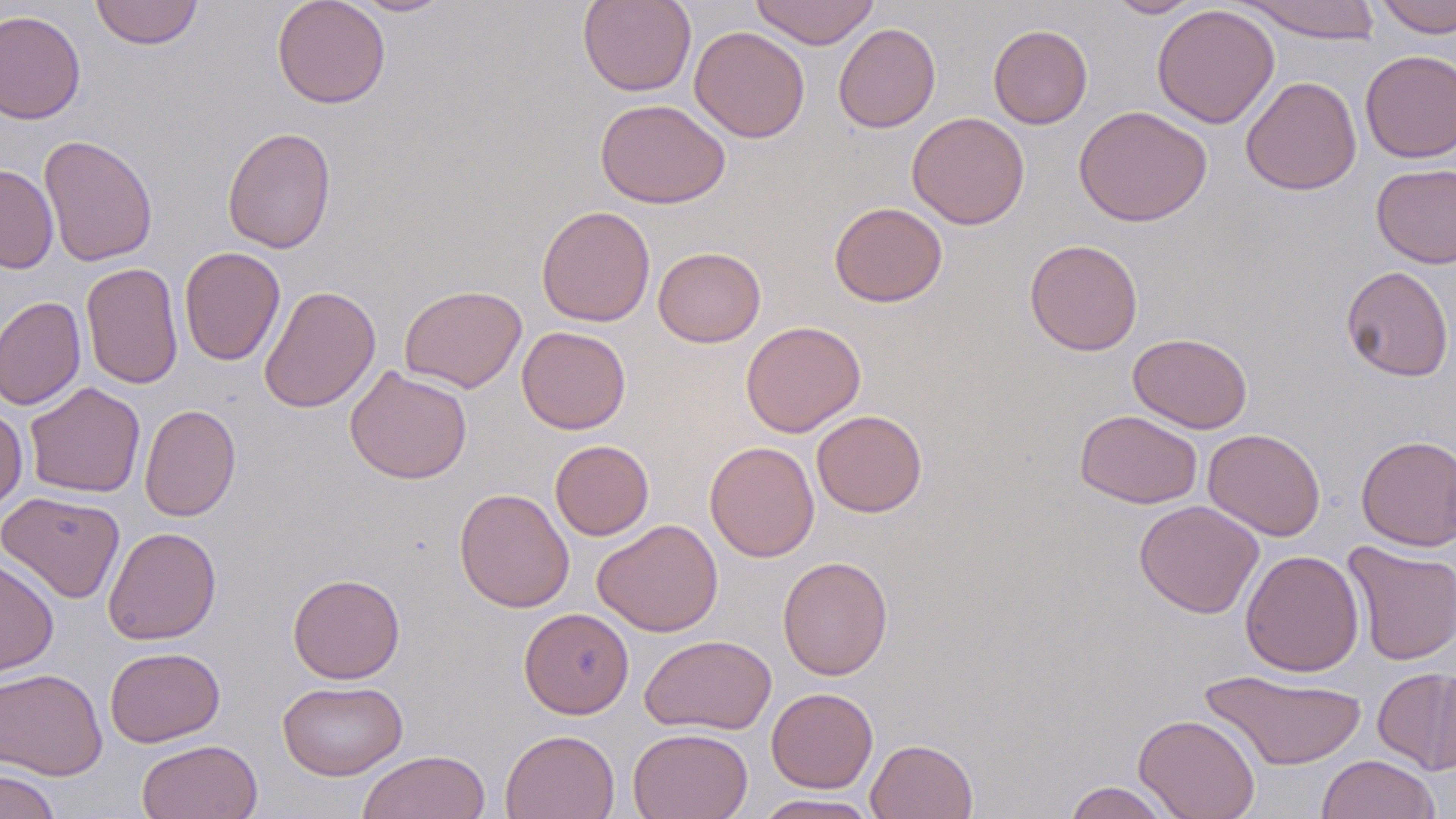
Summary:
  - Coordinate format: approximate bounding boxes as (x1,y1)-(x2,y2) corner pairs in pixels
  - Uninfected red blood cell locations: (89,0)-(204,49), (272,0)-(391,109), (348,0)-(456,16), (577,0)-(696,97), (750,0)-(880,49), (1106,0)-(1205,18), (1373,0)-(1456,37), (1235,1)-(1383,44), (1151,4)-(1280,129), (0,9)-(85,125), (833,23)-(941,133), (988,24)-(1092,129), (689,25)-(810,143), (1360,49)-(1456,163), (1240,75)-(1362,196), (595,98)-(731,208), (1073,105)-(1212,227), (906,112)-(1029,229), (222,126)-(337,254), (39,134)-(158,267), (1371,163)-(1456,269), (0,164)-(58,273), (829,201)-(947,307), (535,205)-(655,327), (1025,239)-(1143,356), (179,246)-(284,367), (653,246)-(766,348), (81,262)-(183,390), (1340,265)-(1454,382), (259,285)-(381,413), (399,285)-(527,393), (0,296)-(85,410), (740,320)-(866,438), (517,326)-(631,435), (1128,332)-(1253,433), (345,364)-(472,484), (24,381)-(145,498), (139,404)-(241,522), (0,406)-(28,511), (1075,409)-(1203,509), (811,410)-(927,517), (1203,428)-(1326,540), (1356,434)-(1456,551), (550,440)-(654,540), (704,441)-(820,562), (454,487)-(575,613), (0,491)-(126,603), (1134,499)-(1264,619), (592,519)-(723,637), (102,526)-(222,644), (1343,541)-(1456,666), (1240,549)-(1364,676), (0,555)-(59,677), (777,556)-(893,680), (287,572)-(405,684), (519,607)-(634,719), (639,634)-(777,735), (104,646)-(225,747), (1373,666)-(1456,775), (0,668)-(108,780), (1200,668)-(1368,771), (277,679)-(408,780), (766,687)-(878,793), (1133,714)-(1261,819), (628,727)-(753,819), (499,729)-(620,819), (865,738)-(978,819), (136,739)-(263,819), (356,750)-(490,819), (1317,754)-(1441,819), (0,768)-(61,819), (1062,781)-(1176,818), (753,794)-(880,818)
  - Slide-level diagnosis: negative for blood parasites
  - Image size: 1456×819 pixels
  - Stain: May-Grünwald-Giemsa
  - Preparation: thin blood smear
  - Magnification: 1000x
  - Field of view: one of a larger specimen
  - Modality: optical microscopy